Assess this cell for malaria.
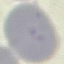
Uninfected.

Summary:
  - Image type: cell patch, automatically extracted from a larger field of view and resized to 64 × 64 pixels
  - Preparation: thin blood smear
  - Capture: smartphone through the microscope eyepiece
  - Stain: Giemsa